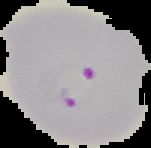

Summary:
  - Preparation: thin blood smear
  - Image size: 151×148 pixels
  - Image type: segmented cell region on a black background
  - Result: malaria parasites identified